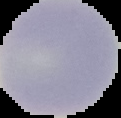
Summary:
  - Result: negative for Plasmodium parasites
  - Image size: 121×118 pixels
  - Preparation: thin blood film
  - Image type: segmented cell region on a black background